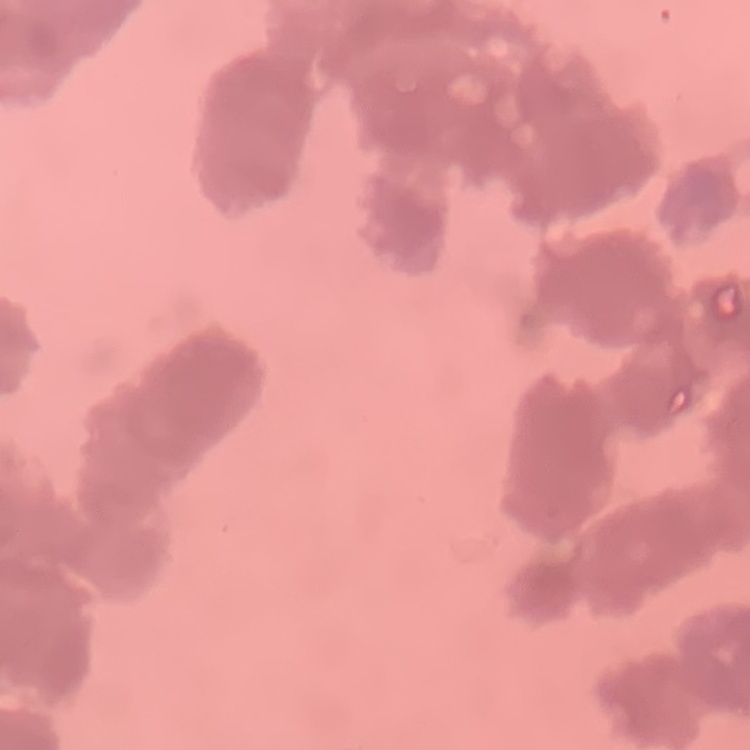
The red blood cells show rouleaux formation. One tile cut from a larger photomicrograph. Stained with either Field's or Giemsa. Thin peripheral smear.